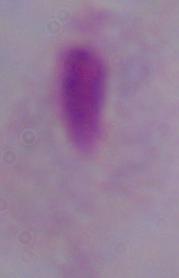

Summary:
  - Magnification: 1000x
  - Modality: photomicrograph
  - Identification: trichomonad